Identify the preparation type.
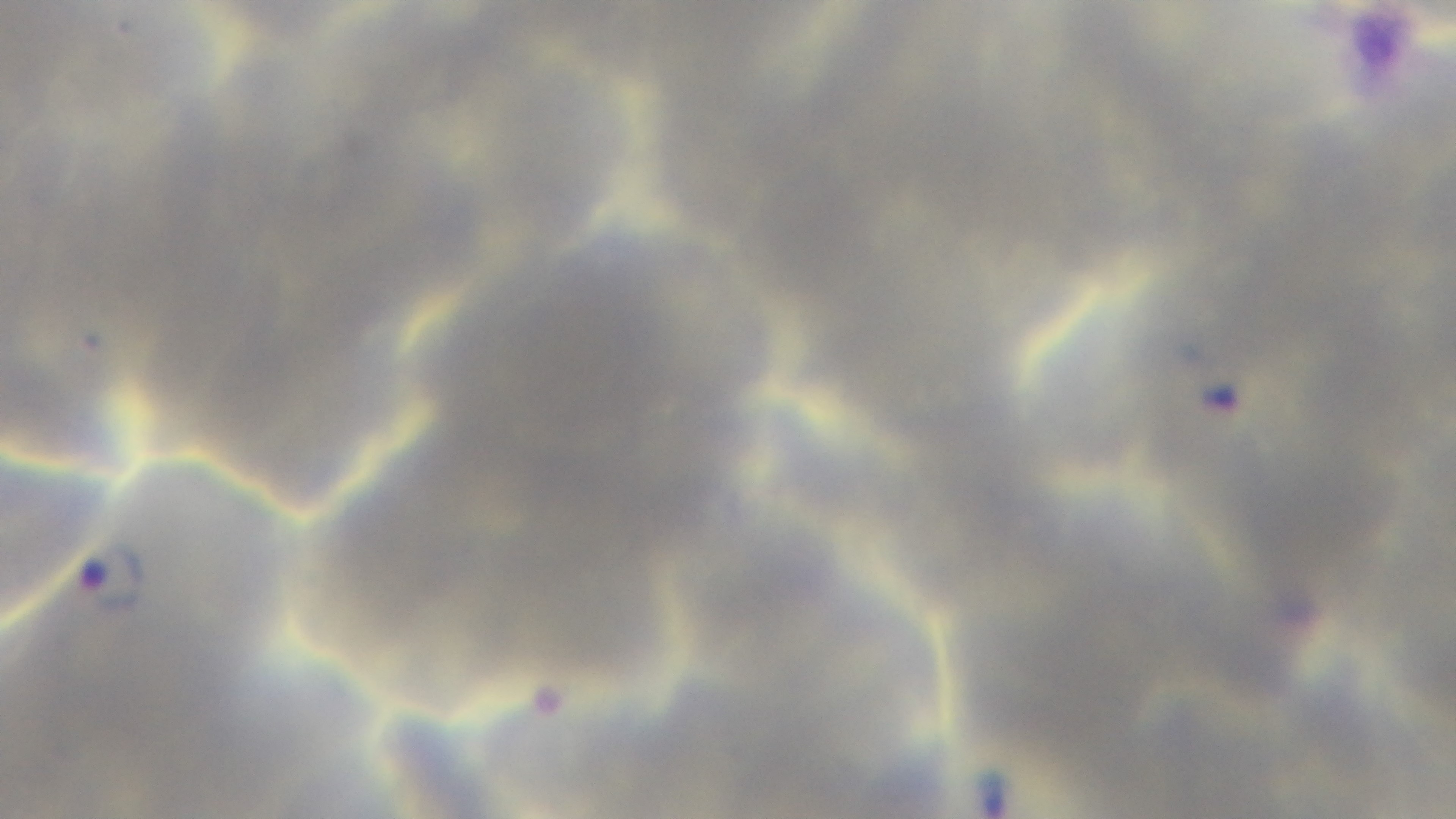
Thin.

objective = 100x oil immersion
modality = light microscopy
stain = Giemsa
capture = mounted 4K digital camera
field of view = one from the slide
malaria status = infected